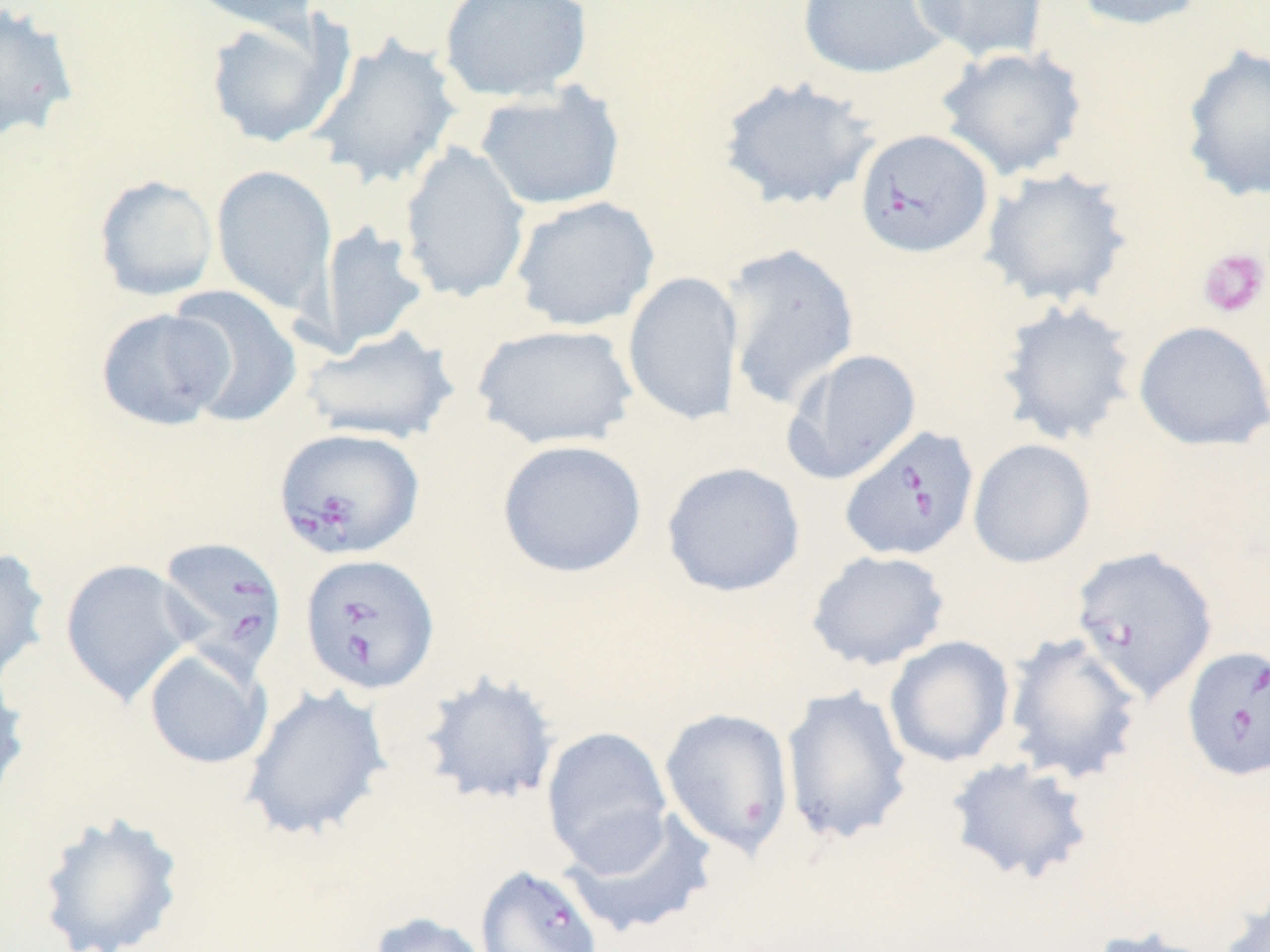
Approximate bounding boxes as named x1/y1/x2/y2 corners in pixels. Babesia divergens-infected red blood cell locations: (x1=854, y1=128, x2=994, y2=259), (x1=839, y1=425, x2=980, y2=562), (x1=273, y1=427, x2=426, y2=560), (x1=156, y1=535, x2=288, y2=679), (x1=299, y1=552, x2=441, y2=695), (x1=1181, y1=645, x2=1270, y2=781), (x1=474, y1=864, x2=604, y2=952). Uninfected red blood cell locations: (x1=177, y1=0, x2=323, y2=39), (x1=438, y1=0, x2=593, y2=103), (x1=797, y1=0, x2=950, y2=80), (x1=911, y1=0, x2=1049, y2=64), (x1=1069, y1=0, x2=1210, y2=32), (x1=0, y1=2, x2=80, y2=143), (x1=204, y1=14, x2=348, y2=149), (x1=307, y1=33, x2=463, y2=191), (x1=1179, y1=43, x2=1270, y2=204), (x1=936, y1=46, x2=1089, y2=181), (x1=716, y1=76, x2=881, y2=212), (x1=474, y1=82, x2=626, y2=211), (x1=398, y1=143, x2=531, y2=304), (x1=211, y1=164, x2=337, y2=314), (x1=979, y1=166, x2=1133, y2=308), (x1=93, y1=174, x2=218, y2=301), (x1=510, y1=195, x2=660, y2=332), (x1=316, y1=221, x2=430, y2=353), (x1=721, y1=242, x2=862, y2=411), (x1=622, y1=271, x2=744, y2=427), (x1=166, y1=284, x2=303, y2=427), (x1=995, y1=298, x2=1139, y2=447), (x1=95, y1=307, x2=234, y2=431), (x1=1133, y1=320, x2=1270, y2=451), (x1=472, y1=323, x2=638, y2=450), (x1=302, y1=326, x2=459, y2=445), (x1=782, y1=347, x2=922, y2=485), (x1=967, y1=438, x2=1096, y2=569), (x1=496, y1=439, x2=647, y2=578), (x1=661, y1=461, x2=806, y2=597), (x1=0, y1=546, x2=52, y2=688), (x1=1070, y1=546, x2=1218, y2=702), (x1=805, y1=549, x2=951, y2=671), (x1=59, y1=558, x2=197, y2=706), (x1=1002, y1=632, x2=1144, y2=785), (x1=884, y1=635, x2=1015, y2=768), (x1=144, y1=647, x2=272, y2=770), (x1=0, y1=668, x2=31, y2=811), (x1=416, y1=668, x2=562, y2=808), (x1=240, y1=683, x2=393, y2=842), (x1=780, y1=684, x2=913, y2=846), (x1=659, y1=706, x2=795, y2=859), (x1=541, y1=726, x2=673, y2=871), (x1=944, y1=756, x2=1095, y2=885), (x1=561, y1=807, x2=719, y2=938), (x1=35, y1=809, x2=187, y2=952), (x1=1219, y1=888, x2=1270, y2=952), (x1=366, y1=911, x2=493, y2=952), (x1=1082, y1=925, x2=1230, y2=952). Platelet locations: (x1=1198, y1=247, x2=1269, y2=319). Slide-level diagnosis: Babesia divergens. Image is 1270×952 pixels. Optical microscopy. Thin blood smear. May-Grünwald-Giemsa-stained preparation. Single field of view. Captured at 1000x magnification.